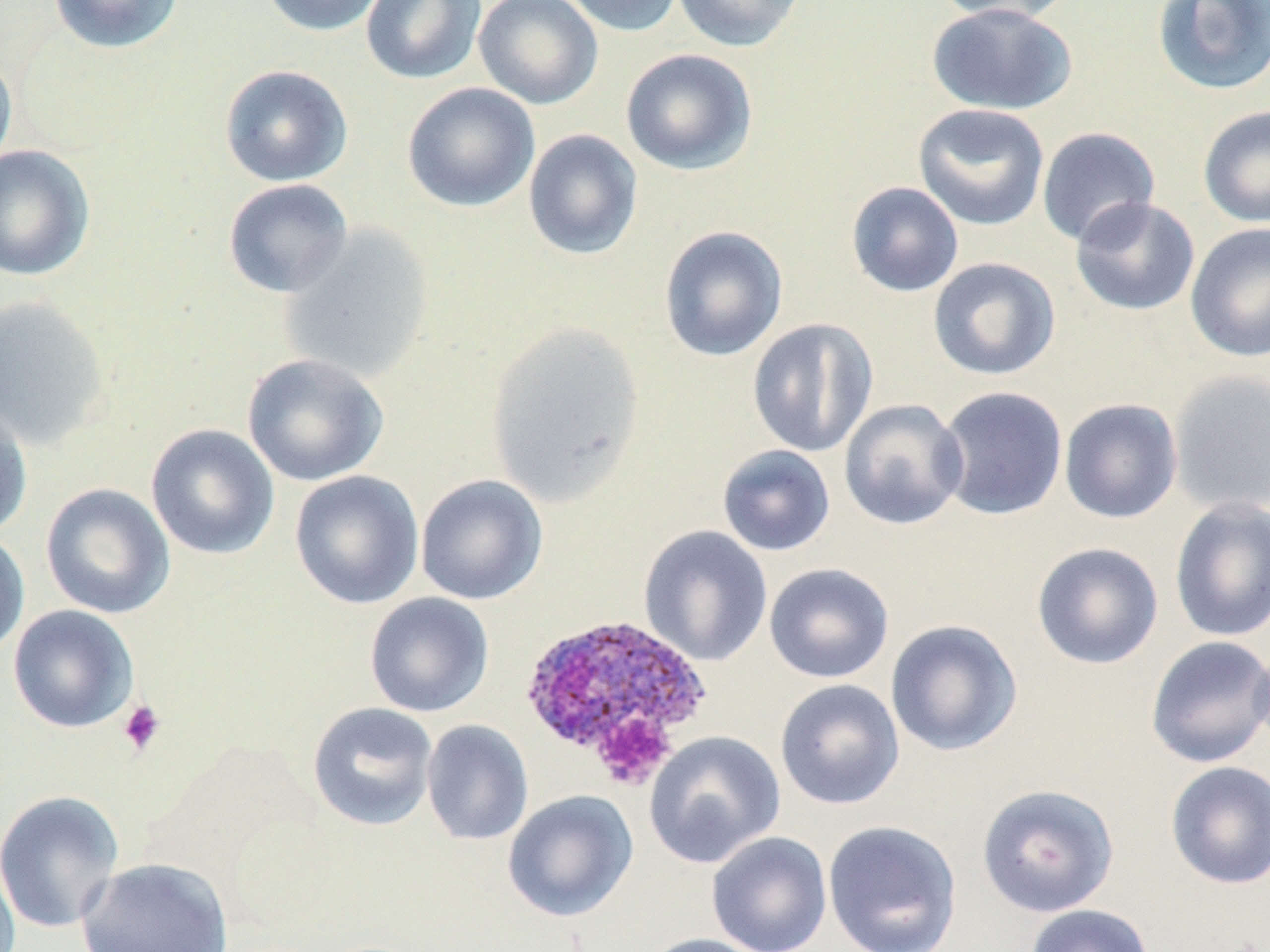
Summary:
  - Coordinate format: approximate bounding boxes as (x1,y1)-(x2,y2) corner pairs in pixels
  - Plasmodium ovale-infected red blood cell locations: (518,614)-(712,780)
  - Uninfected red blood cell locations: (47,0)-(186,54), (258,0)-(391,36), (360,0)-(487,85), (473,0)-(603,109), (557,0)-(686,37), (670,0)-(807,52), (928,0)-(1076,25), (1152,0)-(1270,97), (926,3)-(1079,115), (0,48)-(18,177), (620,48)-(759,176), (219,64)-(353,186), (402,82)-(540,212), (912,103)-(1050,231), (1198,104)-(1270,228), (1037,126)-(1160,248), (522,129)-(643,261), (0,145)-(95,281), (223,178)-(353,299), (846,181)-(964,298), (1070,196)-(1201,316), (1185,222)-(1270,362), (278,225)-(435,383), (658,225)-(789,362), (927,256)-(1061,381), (0,295)-(111,451), (747,318)-(879,458), (486,321)-(646,506), (241,353)-(390,487), (1168,369)-(1270,516), (936,385)-(1069,521), (838,398)-(969,531), (1058,398)-(1183,524), (0,402)-(33,538), (145,423)-(280,560), (716,444)-(836,557), (289,470)-(425,610), (415,474)-(548,605), (40,482)-(175,619), (1168,497)-(1270,642), (638,525)-(773,666), (0,529)-(30,660), (1031,541)-(1164,670), (763,562)-(894,684), (364,592)-(494,717), (7,604)-(139,733), (885,619)-(1023,757), (1144,635)-(1270,769), (1251,636)-(1270,760), (774,678)-(905,810), (306,701)-(439,831), (421,719)-(534,846), (643,731)-(786,868), (1164,760)-(1270,890), (976,783)-(1120,918), (0,789)-(124,934), (502,790)-(639,923), (822,820)-(962,952), (706,831)-(832,952), (0,842)-(20,952), (76,857)-(234,952), (1024,904)-(1155,952), (636,933)-(772,952)
  - Platelet locations: (117,699)-(167,756), (586,710)-(677,790)
  - Slide-level diagnosis: Plasmodium ovale
  - Stain: May-Grünwald-Giemsa
  - Image size: 1270×952 pixels
  - Magnification: 1000x
  - Field of view: single
  - Preparation: thin blood film
  - Modality: optical microscopy